Report the malaria status of this cell.
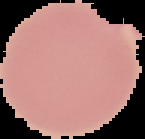
It is uninfected.

Summary:
  - Image type: segmented cell region with the area outside set to black
  - Image size: 145×139 pixels
  - Preparation: thin blood smear